Locate platelets.
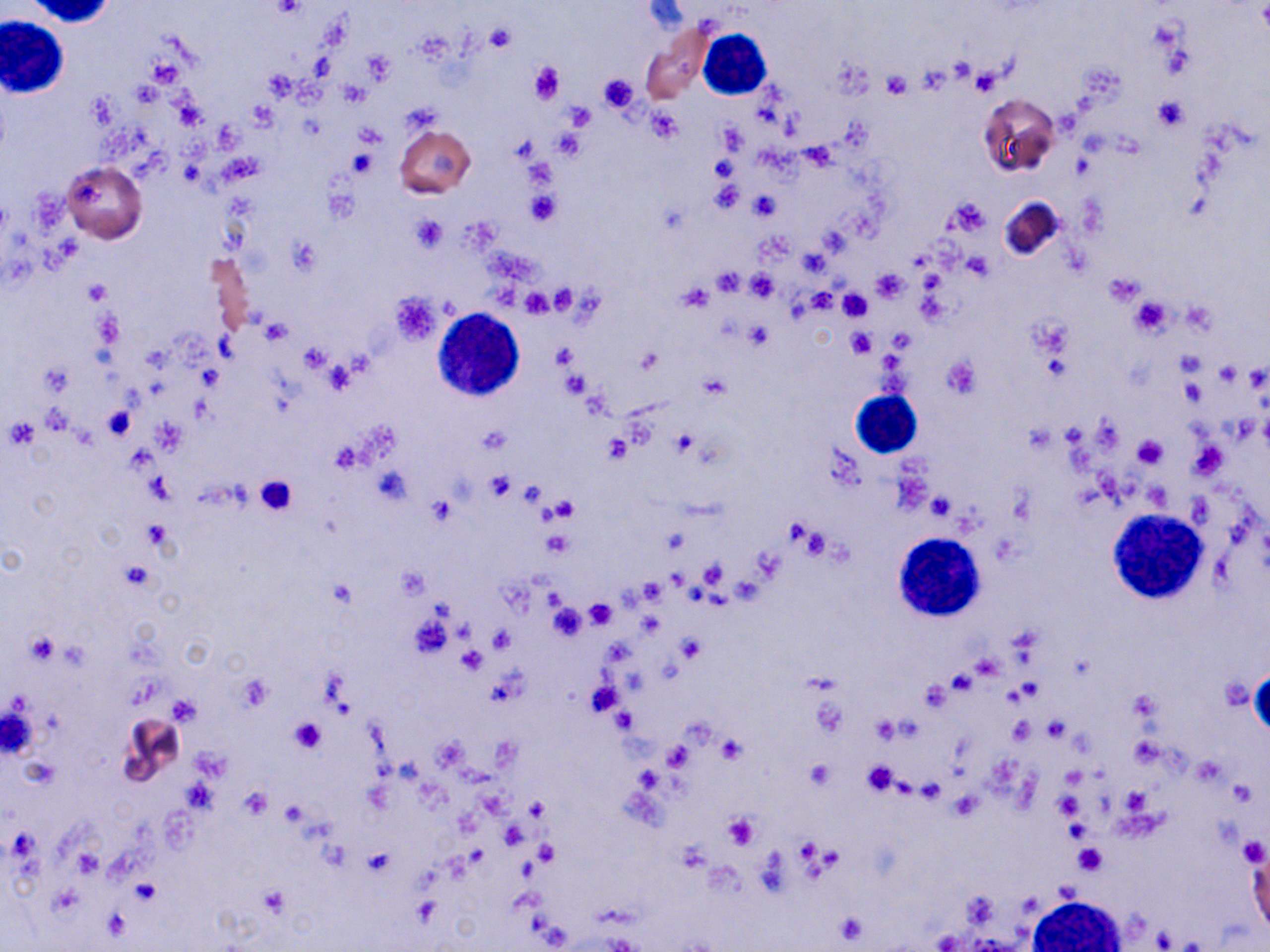

Approximate bounding boxes as (x1,y1)-(x2,y2) corner pairs in pixels.
Platelets: (269,1)-(306,19), (486,25)-(516,51), (363,52)-(394,82), (529,62)-(563,104), (972,67)-(1003,95), (881,71)-(911,97), (598,74)-(638,113), (340,81)-(369,107), (1153,97)-(1189,131), (564,102)-(595,130), (649,109)-(682,141), (719,124)-(748,155), (553,130)-(584,160), (710,156)-(737,183), (708,184)-(743,215), (526,190)-(560,226), (751,190)-(780,222), (947,196)-(992,236), (409,215)-(447,254), (965,253)-(994,279), (712,269)-(744,296), (872,269)-(908,302), (745,271)-(778,302), (1104,272)-(1145,306), (84,278)-(112,304), (677,285)-(714,311), (549,286)-(577,313), (522,289)-(553,317), (839,289)-(873,320), (804,290)-(837,314), (391,292)-(441,345), (1130,298)-(1172,337), (1031,316)-(1072,360), (260,320)-(291,345), (744,322)-(773,351), (848,329)-(876,357), (635,350)-(661,374), (942,356)-(981,397), (1216,361)-(1237,383), (42,363)-(70,395), (563,370)-(588,400), (103,406)-(133,439), (479,428)-(510,454), (672,431)-(697,457), (602,434)-(633,463), (1131,434)-(1168,469), (1193,441)-(1226,481), (484,474)-(516,500), (253,476)-(297,517), (517,483)-(545,505), (927,494)-(952,520), (427,496)-(455,526), (549,498)-(578,523), (543,530)-(574,557), (118,561)-(154,592), (638,576)-(669,603), (584,599)-(616,628), (549,603)-(589,640), (489,625)-(516,651), (28,632)-(59,666), (679,637)-(705,663), (458,647)-(486,674), (237,675)-(272,713), (1,700)-(41,759), (611,708)-(637,733), (288,715)-(327,754), (872,717)-(900,744), (1007,717)-(1034,744), (717,735)-(747,763), (663,743)-(693,771), (807,762)-(834,789), (861,762)-(898,795), (241,789)-(270,819), (1054,790)-(1085,822), (948,792)-(982,821), (524,798)-(548,823), (722,811)-(761,849), (1238,836)-(1267,868), (536,841)-(559,865), (1073,843)-(1108,876), (362,845)-(395,876), (133,878)-(160,907), (260,885)-(288,916), (833,910)-(871,946).

{
  "slide_level_diagnosis": "no evidence of blood parasites",
  "modality": "light microscopy",
  "white_blood_cell_locations": "approximate bounding boxes as (x1,y1)-(x2,y2) corner pairs in pixels: (26,0)-(117,26), (2,15)-(68,98), (698,27)-(771,100), (434,309)-(526,402), (849,389)-(922,457), (1108,509)-(1208,604), (896,532)-(984,621), (1030,895)-(1123,951)",
  "field_of_view": "single",
  "image_size": "1270×952 pixels",
  "preparation": "thin blood smear",
  "stain": "May-Grünwald-Giemsa",
  "uninfected_red_blood_cell_locations": "approximate bounding boxes as (x1,y1)-(x2,y2) corner pairs in pixels: (977,92)-(1060,177), (395,125)-(476,198), (62,161)-(148,243), (998,195)-(1068,263), (208,251)-(257,338), (1192,439)-(1228,480), (117,712)-(187,791), (1247,842)-(1267,934)",
  "magnification": "1000x"
}